Give the position of every Plasmodium parasite.
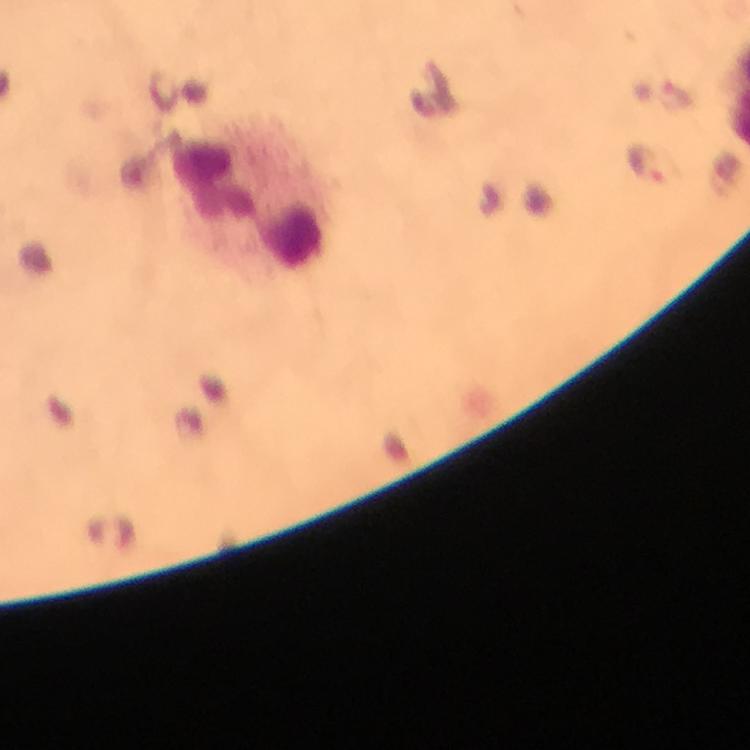

Approximate centers as (x, y) in pixels.
Plasmodium parasites: (680, 97), (646, 163).

Leukocyte locations: (246, 201). Smartphone photograph taken through a microscope. At 100x magnification. From a diagnostic examination for malaria. Thick blood film. Image is 750×750 pixels. Cropped region of a single field of view. Giemsa stain. Immersion oil was used.